Report the malaria status of this cell.
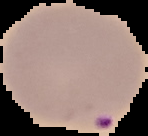

It is parasitized.

Summary:
  - Image type: cell region segmented out of the field of view; surrounding area masked to black
  - Preparation: thin blood film
  - Image size: 148×136 pixels